Classify this cell by malaria status.
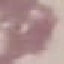

It is uninfected.

Summary:
  - Preparation: thin smear
  - Stain: Giemsa
  - Image type: automatically extracted cell patch, resized to 64 × 64 pixels
  - Capture: smartphone camera at the microscope eyepiece